Locate every uninfected red blood cell.
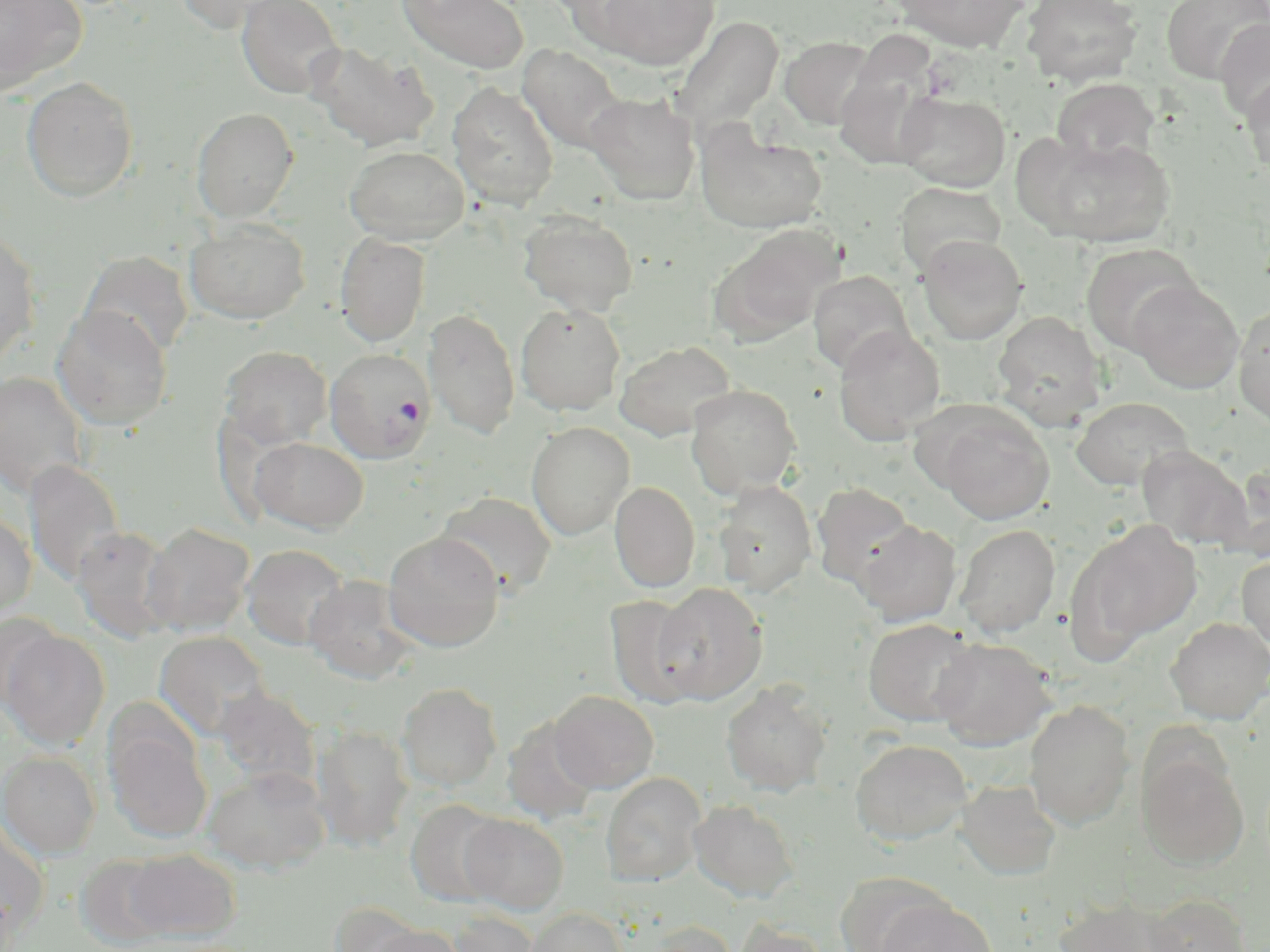

Approximate bounding boxes as (x1, y1, x2, y2) in pixels.
Uninfected red blood cells: (0, 0, 87, 94), (172, 0, 291, 33), (236, 0, 345, 100), (397, 0, 529, 73), (590, 0, 719, 71), (889, 0, 1031, 52), (1021, 0, 1144, 87), (1161, 0, 1269, 84), (669, 16, 784, 144), (1214, 18, 1270, 124), (780, 36, 877, 130), (305, 41, 439, 152), (517, 44, 627, 154), (834, 52, 941, 170), (1241, 70, 1270, 175), (20, 76, 139, 202), (1052, 78, 1160, 168), (447, 82, 560, 210), (584, 91, 701, 206), (894, 91, 1010, 191), (191, 106, 299, 222), (695, 127, 827, 233), (1030, 134, 1177, 248), (344, 144, 469, 244), (894, 182, 1006, 277), (519, 211, 639, 317), (184, 219, 310, 324), (713, 226, 841, 345), (0, 227, 42, 369), (335, 231, 431, 347), (917, 234, 1028, 345), (1080, 242, 1201, 355), (79, 250, 193, 359), (808, 271, 914, 376), (1128, 279, 1245, 393), (516, 302, 626, 416), (1232, 302, 1270, 430), (51, 306, 172, 430), (423, 307, 520, 440), (991, 311, 1107, 429), (833, 326, 945, 446), (615, 340, 737, 441), (220, 346, 333, 450), (1, 371, 90, 500), (685, 383, 802, 497), (1071, 397, 1194, 492), (929, 407, 1055, 525), (526, 421, 635, 540), (250, 437, 368, 534), (1136, 445, 1253, 550), (23, 459, 126, 587), (1218, 462, 1270, 562), (713, 480, 817, 596), (609, 481, 700, 593), (811, 483, 915, 587), (437, 491, 556, 597), (0, 510, 37, 621), (1068, 519, 1201, 652), (855, 520, 963, 626), (142, 522, 255, 637), (955, 524, 1060, 637), (71, 526, 177, 643), (383, 530, 505, 653), (241, 544, 353, 651), (1236, 553, 1270, 651), (303, 574, 421, 684), (651, 581, 767, 704), (604, 595, 705, 708), (0, 613, 64, 709), (1165, 617, 1270, 724), (862, 619, 979, 726), (0, 628, 110, 750), (153, 630, 272, 741), (930, 637, 1056, 751), (721, 681, 833, 797), (397, 682, 503, 792), (212, 688, 320, 790), (548, 690, 659, 793), (1025, 701, 1135, 829), (501, 717, 600, 826), (105, 722, 212, 843), (311, 724, 414, 853), (851, 739, 973, 845), (1137, 750, 1250, 871), (0, 751, 101, 858), (203, 765, 331, 874), (600, 772, 706, 887), (956, 780, 1061, 881), (404, 799, 508, 908), (688, 799, 800, 903), (459, 814, 568, 915), (0, 820, 51, 944), (124, 849, 240, 941), (76, 855, 173, 947), (833, 872, 950, 951), (1146, 894, 1251, 952), (875, 897, 998, 952), (1054, 897, 1184, 952), (330, 901, 428, 951), (524, 907, 629, 952), (440, 909, 542, 952), (731, 919, 830, 952), (639, 921, 740, 952), (363, 923, 465, 952).

slide-level diagnosis = Plasmodium falciparum
magnification = 1000x
stain = May-Grünwald-Giemsa
image size = 1270×952 pixels
modality = optical microscopy
field of view = single
preparation = thin blood film
Plasmodium falciparum-infected red blood cell locations = approximate bounding boxes as (x1, y1, x2, y2) in pixels: (325, 348, 434, 463)